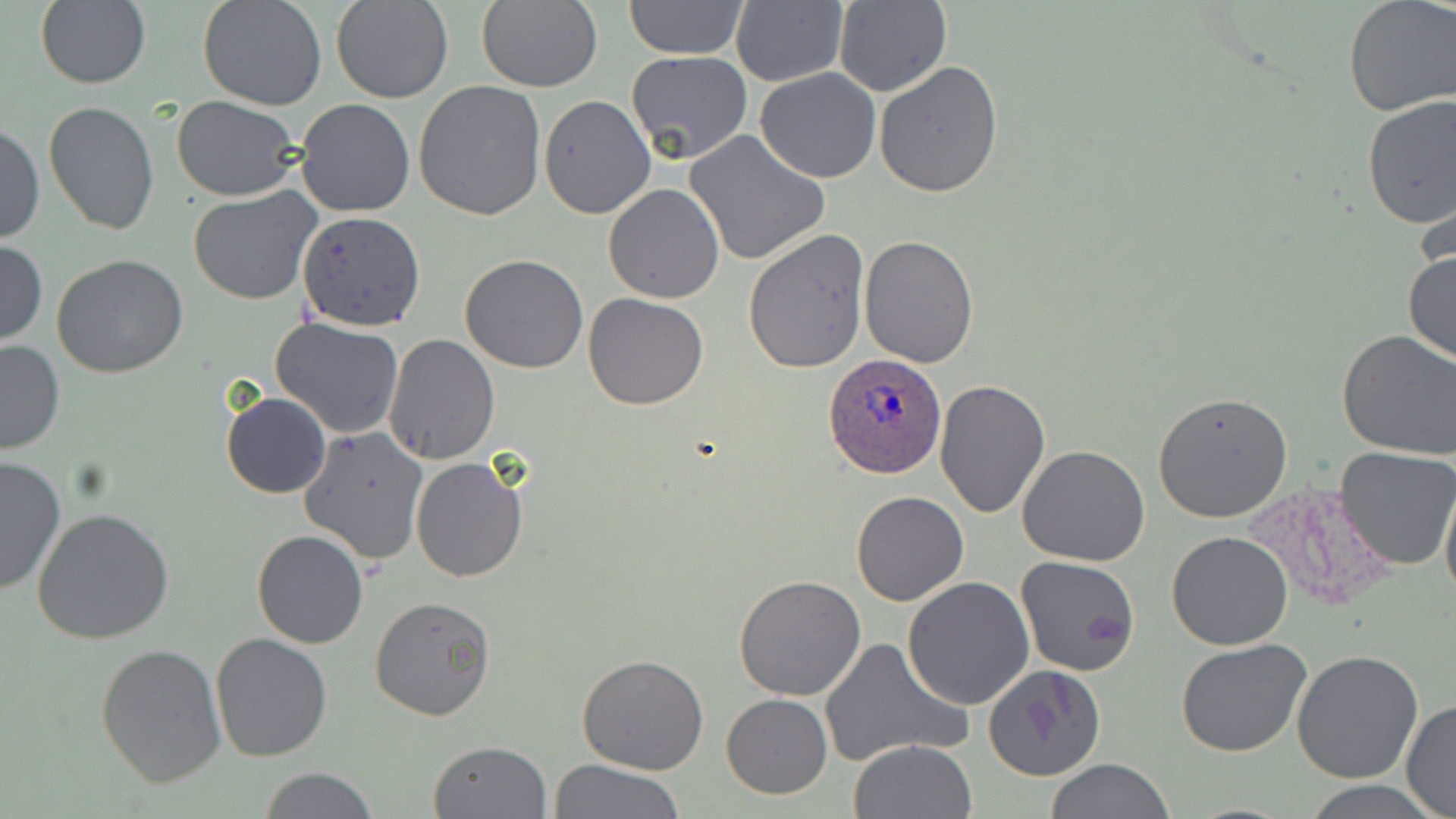 Approximate bounding boxes as named x1/y1/x2/y2 corners in pixels. Uninfected red blood cell locations: (x1=330, y1=0, x2=455, y2=104), (x1=623, y1=0, x2=748, y2=60), (x1=1342, y1=0, x2=1456, y2=118), (x1=33, y1=1, x2=150, y2=89), (x1=198, y1=1, x2=328, y2=111), (x1=475, y1=1, x2=602, y2=92), (x1=834, y1=1, x2=951, y2=97), (x1=731, y1=3, x2=847, y2=86), (x1=624, y1=51, x2=752, y2=167), (x1=874, y1=61, x2=1004, y2=198), (x1=755, y1=68, x2=882, y2=183), (x1=413, y1=78, x2=547, y2=221), (x1=709, y1=82, x2=865, y2=235), (x1=1359, y1=93, x2=1456, y2=230), (x1=539, y1=95, x2=655, y2=219), (x1=173, y1=96, x2=304, y2=201), (x1=296, y1=99, x2=416, y2=219), (x1=43, y1=101, x2=160, y2=235), (x1=1, y1=120, x2=43, y2=248), (x1=685, y1=131, x2=829, y2=266), (x1=604, y1=183, x2=724, y2=302), (x1=189, y1=187, x2=320, y2=306), (x1=297, y1=210, x2=425, y2=331), (x1=743, y1=230, x2=869, y2=372), (x1=859, y1=235, x2=979, y2=369), (x1=0, y1=240, x2=47, y2=344), (x1=1403, y1=246, x2=1456, y2=368), (x1=51, y1=253, x2=189, y2=377), (x1=460, y1=254, x2=588, y2=373), (x1=583, y1=293, x2=709, y2=409), (x1=270, y1=318, x2=404, y2=440), (x1=1337, y1=329, x2=1456, y2=459), (x1=384, y1=332, x2=499, y2=465), (x1=0, y1=339, x2=64, y2=456), (x1=934, y1=380, x2=1051, y2=519), (x1=1152, y1=391, x2=1293, y2=523), (x1=221, y1=392, x2=331, y2=498), (x1=299, y1=426, x2=428, y2=565), (x1=1017, y1=445, x2=1151, y2=567), (x1=1336, y1=445, x2=1456, y2=569), (x1=0, y1=455, x2=66, y2=597), (x1=409, y1=457, x2=529, y2=581), (x1=1440, y1=471, x2=1456, y2=612), (x1=850, y1=492, x2=969, y2=608), (x1=31, y1=509, x2=174, y2=646), (x1=251, y1=530, x2=368, y2=649), (x1=1166, y1=530, x2=1294, y2=650), (x1=1015, y1=557, x2=1142, y2=676), (x1=733, y1=575, x2=866, y2=701), (x1=902, y1=576, x2=1035, y2=710), (x1=368, y1=596, x2=496, y2=723), (x1=209, y1=632, x2=333, y2=760), (x1=818, y1=637, x2=970, y2=768), (x1=1175, y1=637, x2=1315, y2=756), (x1=96, y1=643, x2=226, y2=786), (x1=1292, y1=648, x2=1423, y2=783), (x1=576, y1=654, x2=710, y2=775), (x1=982, y1=665, x2=1104, y2=781), (x1=722, y1=693, x2=832, y2=799), (x1=1401, y1=700, x2=1456, y2=817), (x1=850, y1=738, x2=978, y2=819), (x1=427, y1=741, x2=549, y2=819), (x1=548, y1=758, x2=683, y2=819), (x1=1047, y1=758, x2=1173, y2=819), (x1=257, y1=767, x2=380, y2=819), (x1=1300, y1=778, x2=1442, y2=818). Plasmodium ovale-infected red blood cell locations: (x1=824, y1=357, x2=946, y2=478). Slide-level diagnosis: Plasmodium ovale. May-Grünwald-Giemsa stain. Captured at 1000x magnification. Light microscopy. One field of a larger specimen. Image is 1456×819 pixels. Thin blood smear.